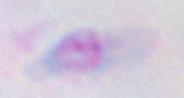

modality: micrograph
magnification: 1000x
identification: Toxoplasma gondii